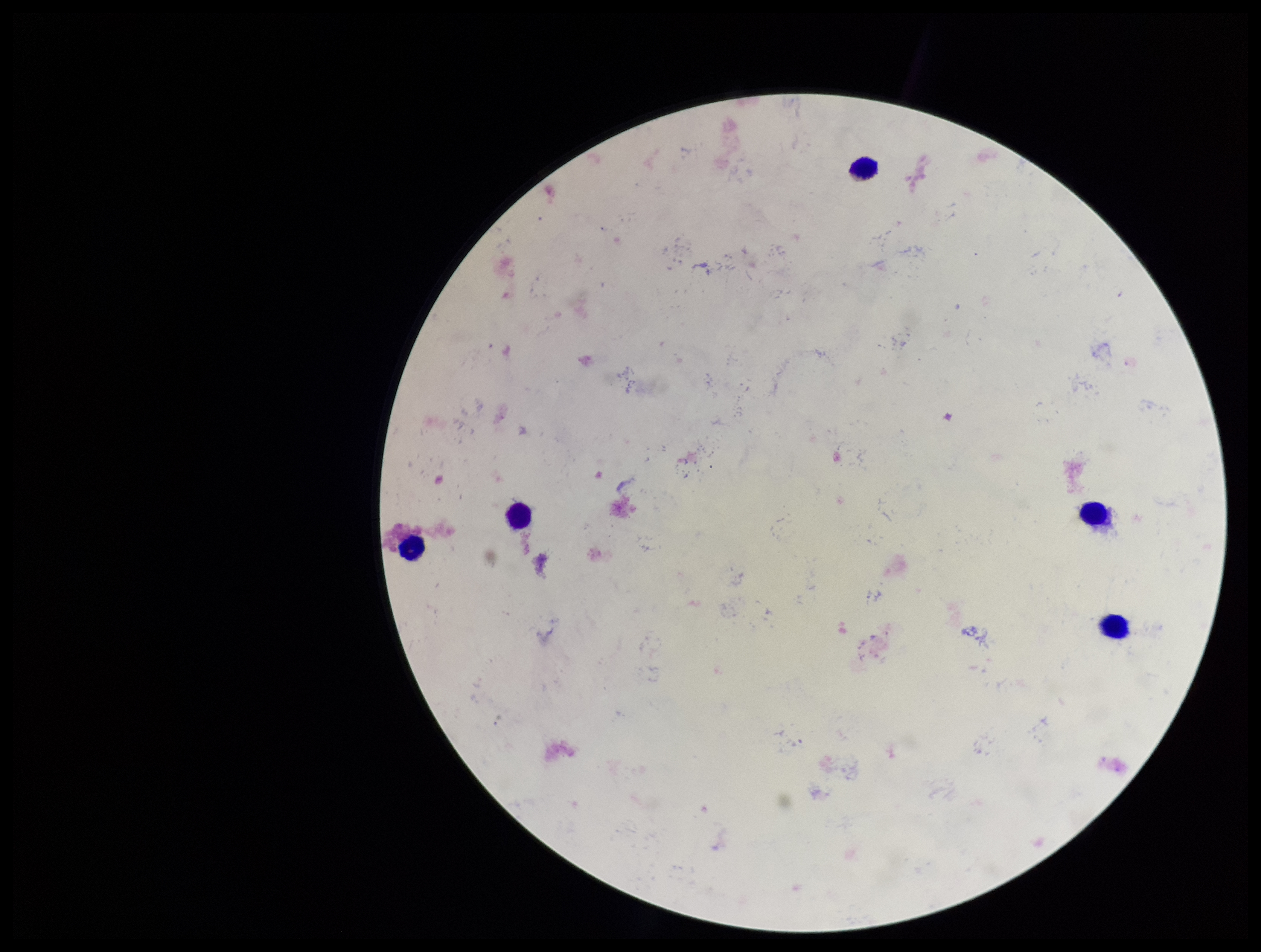
Image is 1261×952 pixels. Parasite count: 0. Plasmodium parasites: none seen. Single field of view. Photographed through the microscope eyepiece with a smartphone camera. Patient malaria status: negative. Giemsa stain. Preparation: thick smear. Leukocyte count: 5.